Describe the morphology of the erythrocytes.
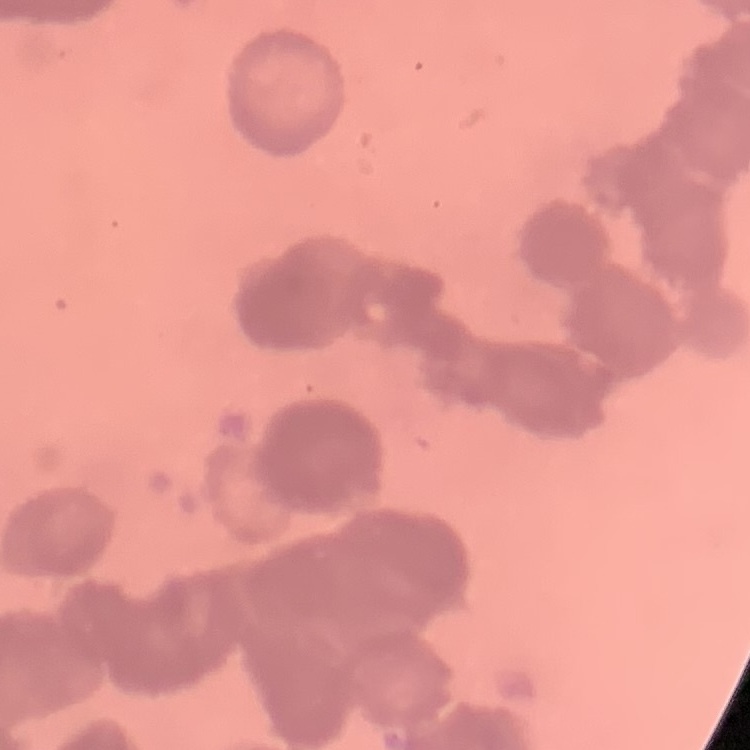

Rouleaux formation.

Summary:
  - Image type: square crop of a larger photomicrograph
  - Stain: Field's or Giemsa
  - Preparation: thin peripheral smear